Comment on the morphology of the red blood cells.
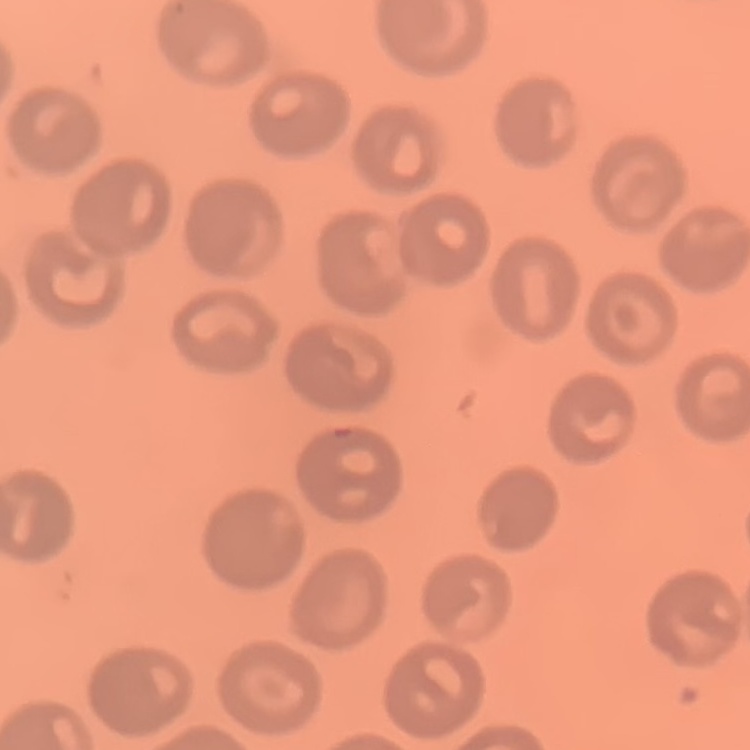
They show no rouleaux formation.

Summary:
  - Image type: one tile cut from a larger photomicrograph
  - Stain: Field's or Giemsa
  - Preparation: thin blood film